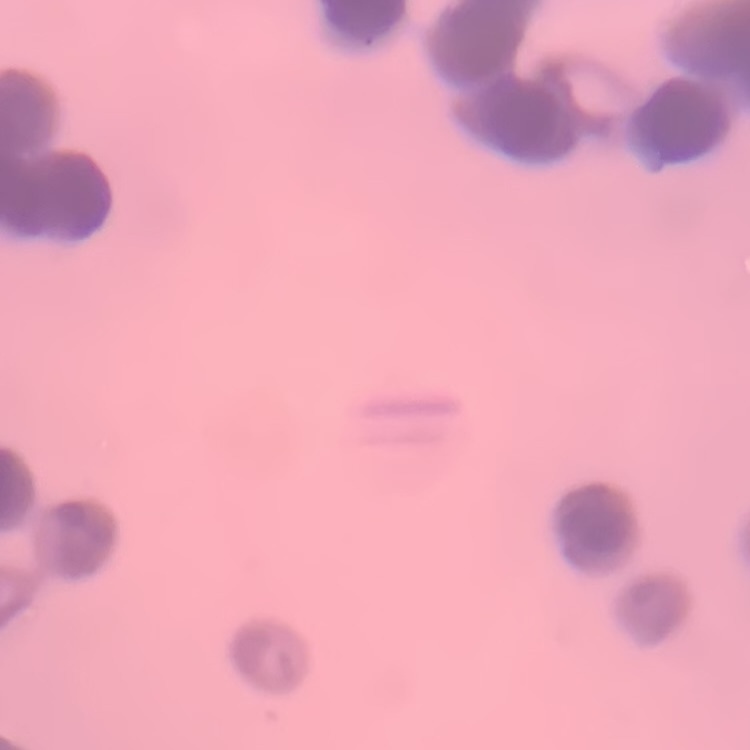

erythrocyte_morphology: rouleaux formation
image_type: one tile cut from a larger photomicrograph
preparation: thin blood film
stain: Field's or Giemsa